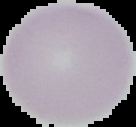
image type = cell region segmented out of the field of view; surrounding area masked to black
result = no malaria parasites detected
preparation = thin blood smear
image size = 136×127 pixels